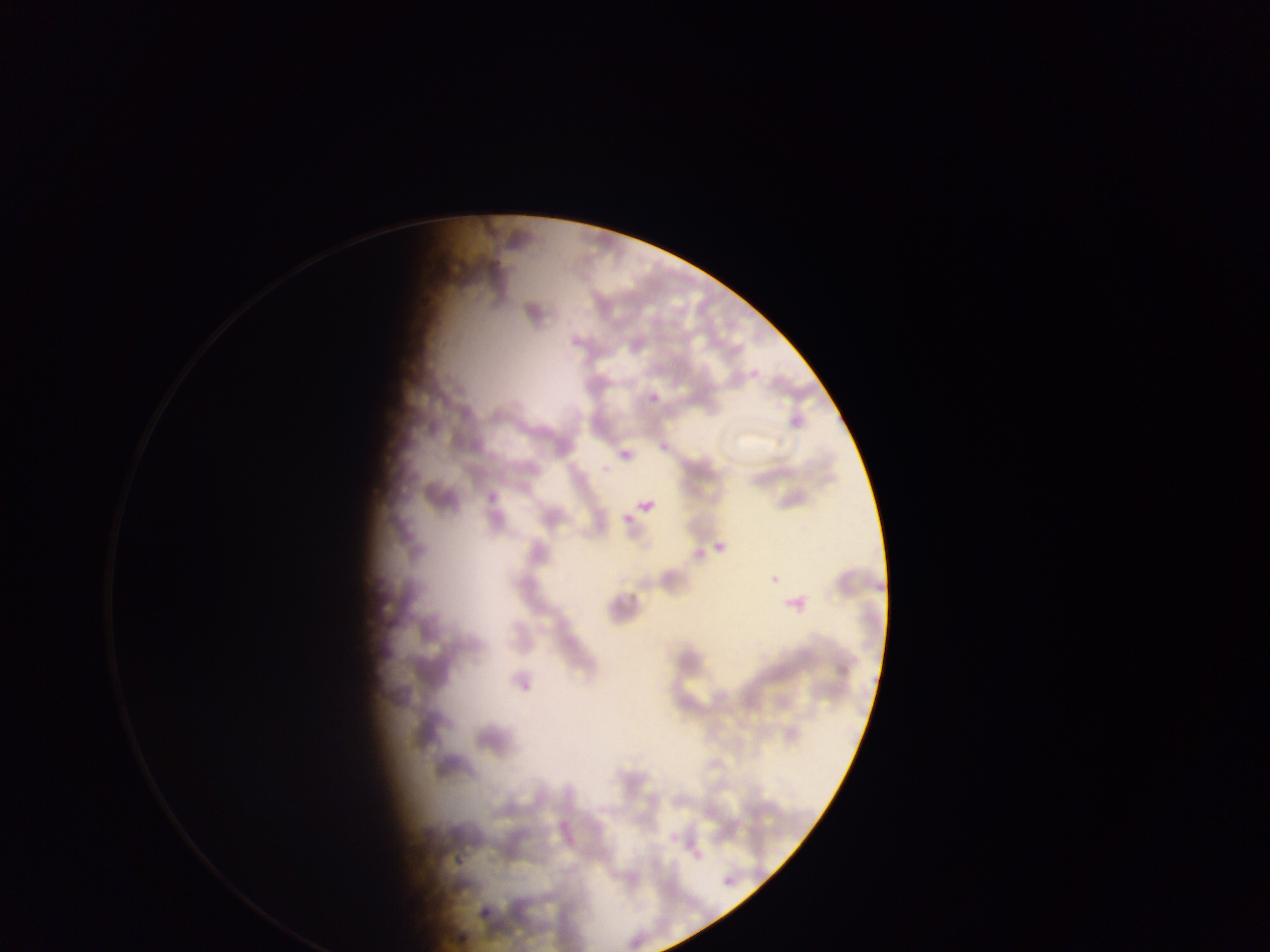
Approximate bounding boxes as {left, top, right, bottom} in pixels. Malaria parasite locations: {649, 392, 660, 402}, {620, 450, 631, 460}, {601, 464, 610, 474}, {637, 504, 664, 516}, {622, 513, 634, 523}, {713, 538, 731, 559}, {785, 590, 812, 619}, {762, 801, 782, 819}, {669, 833, 679, 844}, {451, 845, 470, 876}, {724, 876, 735, 886}, {479, 905, 494, 923}. One field of view. Collected in Ghana. Image is 1270×952 pixels. Mobile-phone photograph taken through the microscope. Thin blood smear.